Identify the parasite.
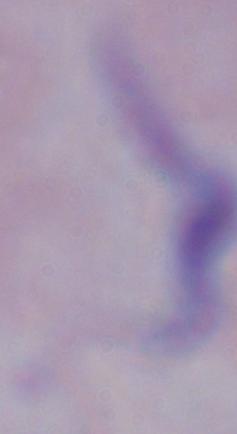
A trypanosome.

{
  "modality": "micrograph",
  "magnification": "1000x"
}